Classify this cell by malaria status.
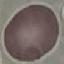

It is uninfected.

{
  "stain": "Giemsa",
  "preparation": "thin smear",
  "capture": "smartphone camera at the microscope eyepiece",
  "image_type": "cell patch, automatically extracted from a larger field of view and resized to 64 × 64 pixels"
}